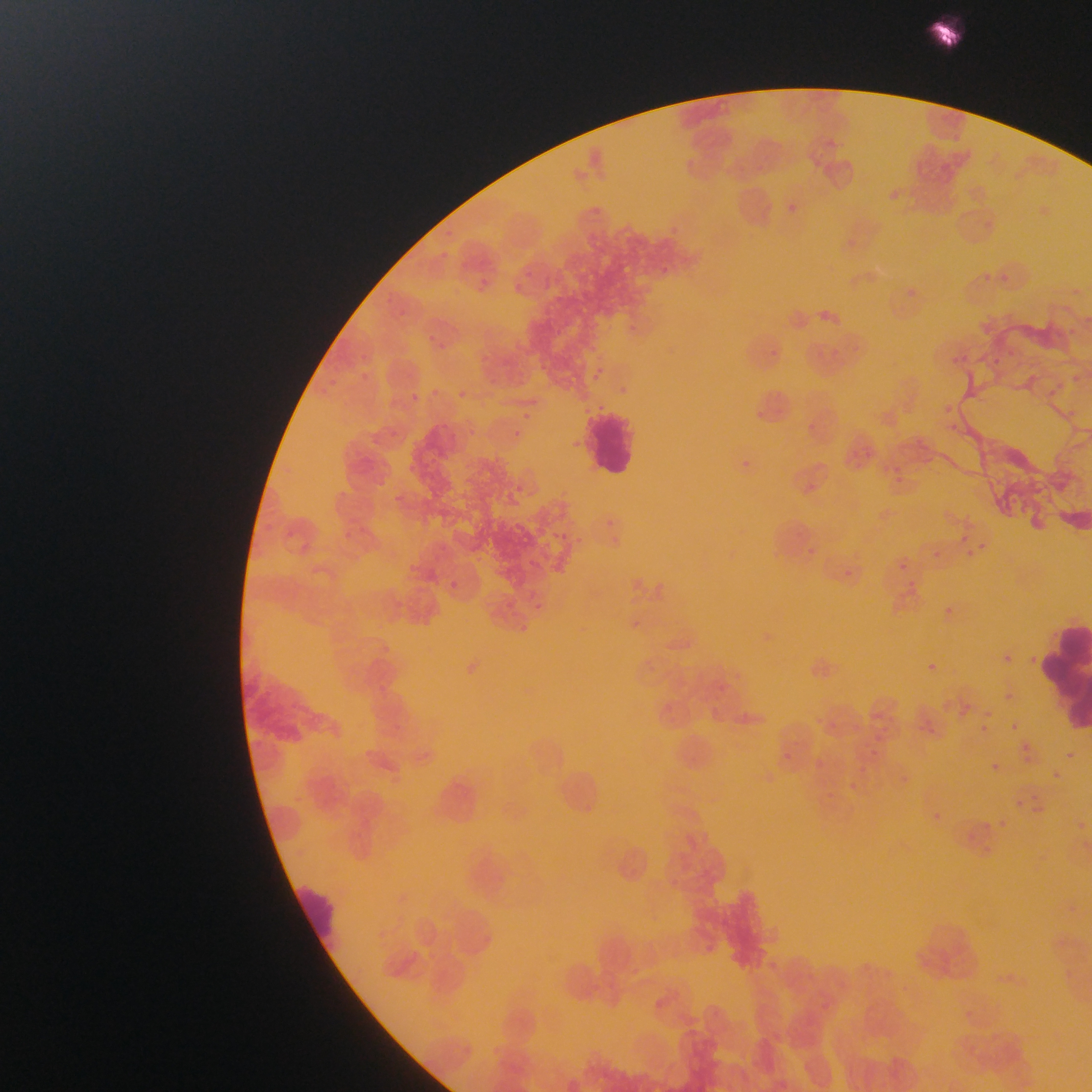
{
  "field_of_view": "single",
  "leukocyte_locations": "approximate bounding boxes as {left, top, right, bottom} in pixels: {590, 405, 639, 495}, {1041, 615, 1092, 728}, {296, 882, 337, 953}",
  "image_size": "1092×1092 pixels",
  "preparation": "thin blood smear",
  "country": "Ghana",
  "capture": "mobile-phone photograph through a microscope"
}